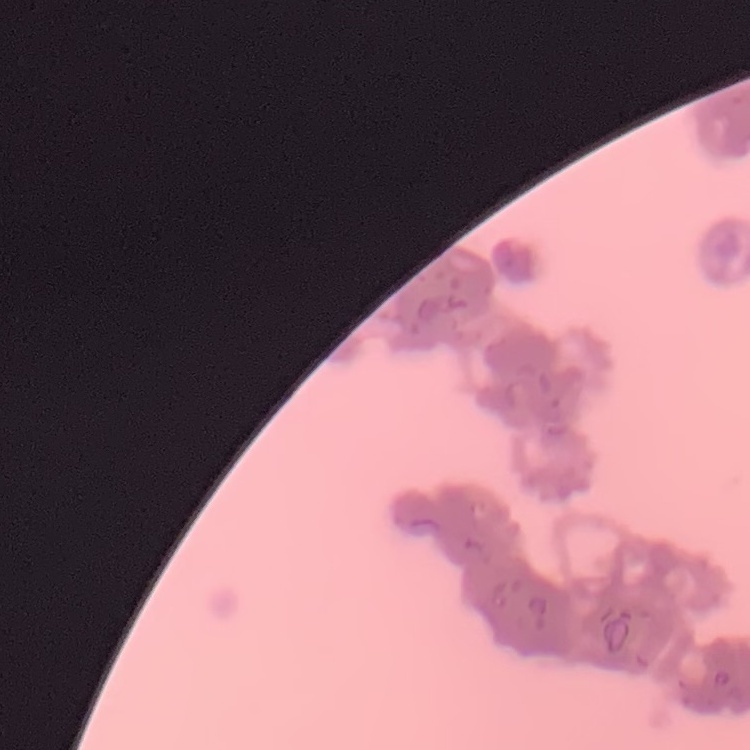
Summary:
  - Erythrocyte morphology: rouleaux formation
  - Image type: one tile cut from a larger photomicrograph
  - Preparation: thin blood smear
  - Stain: Field's or Giemsa